Identify the blood parasite species.
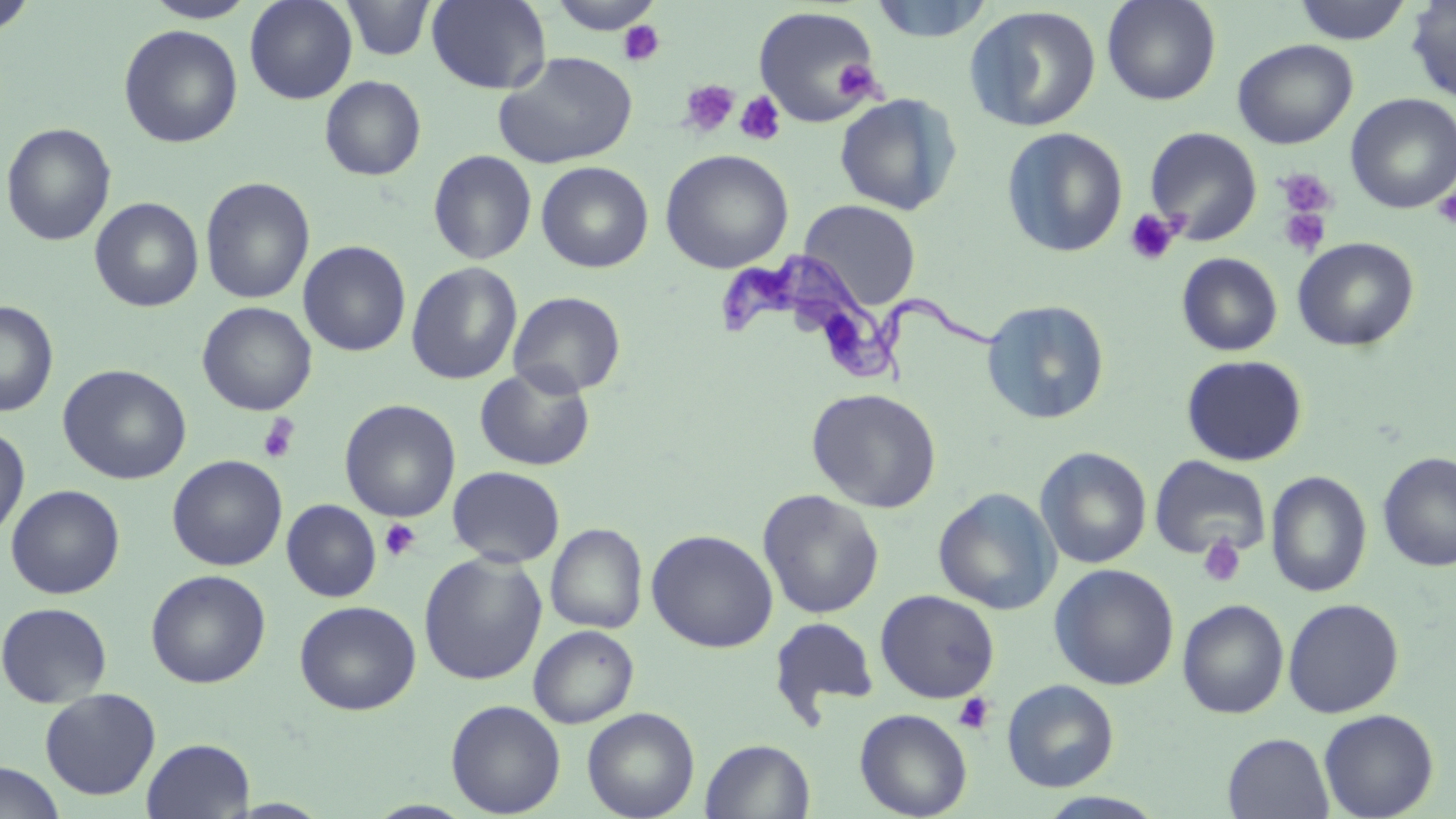

Trypanosoma brucei.

Summary:
  - Coordinate format: approximate bounding boxes as (x1, y1, x2, y2) in pixels
  - Uninfected red blood cell locations: (0, 0, 38, 38), (143, 0, 259, 23), (245, 0, 357, 104), (341, 0, 436, 61), (426, 0, 551, 94), (546, 0, 665, 34), (869, 0, 994, 42), (1102, 0, 1221, 105), (1405, 0, 1456, 103), (1291, 1, 1413, 44), (752, 6, 882, 127), (964, 6, 1102, 132), (119, 24, 242, 148), (1232, 38, 1357, 149), (494, 51, 637, 169), (319, 75, 426, 181), (834, 93, 961, 216), (1346, 93, 1456, 214), (1, 122, 117, 246), (1002, 126, 1128, 258), (1144, 126, 1262, 245), (428, 149, 537, 265), (660, 149, 794, 273), (536, 161, 653, 273), (200, 177, 315, 305), (89, 197, 204, 312), (799, 200, 921, 310), (1292, 237, 1419, 352), (298, 240, 411, 357), (1177, 252, 1282, 356), (406, 262, 523, 385), (508, 291, 626, 398), (982, 299, 1111, 426), (0, 301, 58, 417), (197, 301, 317, 416), (1181, 354, 1307, 466), (57, 364, 192, 485), (474, 366, 596, 472), (806, 387, 942, 513), (340, 399, 461, 522), (0, 426, 30, 541), (1035, 446, 1152, 569), (1377, 451, 1456, 572), (167, 454, 287, 571), (1149, 454, 1272, 560), (447, 466, 565, 567), (1266, 470, 1372, 598), (6, 484, 125, 599), (933, 487, 1061, 615), (757, 489, 885, 620), (282, 499, 382, 602), (546, 523, 648, 634), (646, 529, 778, 653), (418, 552, 547, 685), (1049, 563, 1179, 690), (146, 569, 270, 688), (875, 590, 1000, 703), (1282, 597, 1404, 718), (1177, 598, 1289, 719), (294, 600, 421, 715), (0, 601, 113, 708), (769, 616, 880, 721), (528, 625, 639, 728), (1001, 679, 1119, 792), (39, 687, 161, 800), (445, 699, 566, 817), (582, 707, 700, 819), (854, 708, 973, 819), (1318, 708, 1439, 819), (1223, 733, 1334, 818), (142, 738, 254, 818), (700, 738, 815, 819), (0, 762, 65, 819), (1035, 791, 1170, 818)
  - Platelet locations: (618, 20, 665, 67), (831, 58, 882, 102), (679, 79, 741, 138), (735, 91, 786, 146), (1274, 167, 1338, 220), (1433, 188, 1456, 228), (1277, 206, 1332, 258), (1125, 208, 1182, 265), (258, 414, 299, 463), (380, 519, 421, 561), (1197, 534, 1246, 588), (952, 692, 996, 734)
  - Trypanosoma brucei locations: (715, 247, 1005, 392)
  - Preparation: thin blood film
  - Stain: May-Grünwald-Giemsa
  - Field of view: one of a larger specimen
  - Magnification: 1000x
  - Modality: optical microscopy
  - Image size: 1456×819 pixels